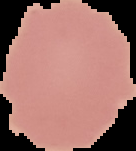
Image is 136×151 pixels. From a thin blood smear. Malaria status: uninfected. Cell region segmented out of the field of view; the surrounding area is masked to black.